Assess this cell for malaria.
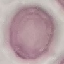

It is uninfected.

Summary:
  - Preparation: thin blood film
  - Capture: smartphone camera at the microscope eyepiece
  - Stain: Giemsa
  - Image type: automatically extracted cell patch, resized to 64 × 64 pixels